Give the position of every Plasmodium parasite visible.
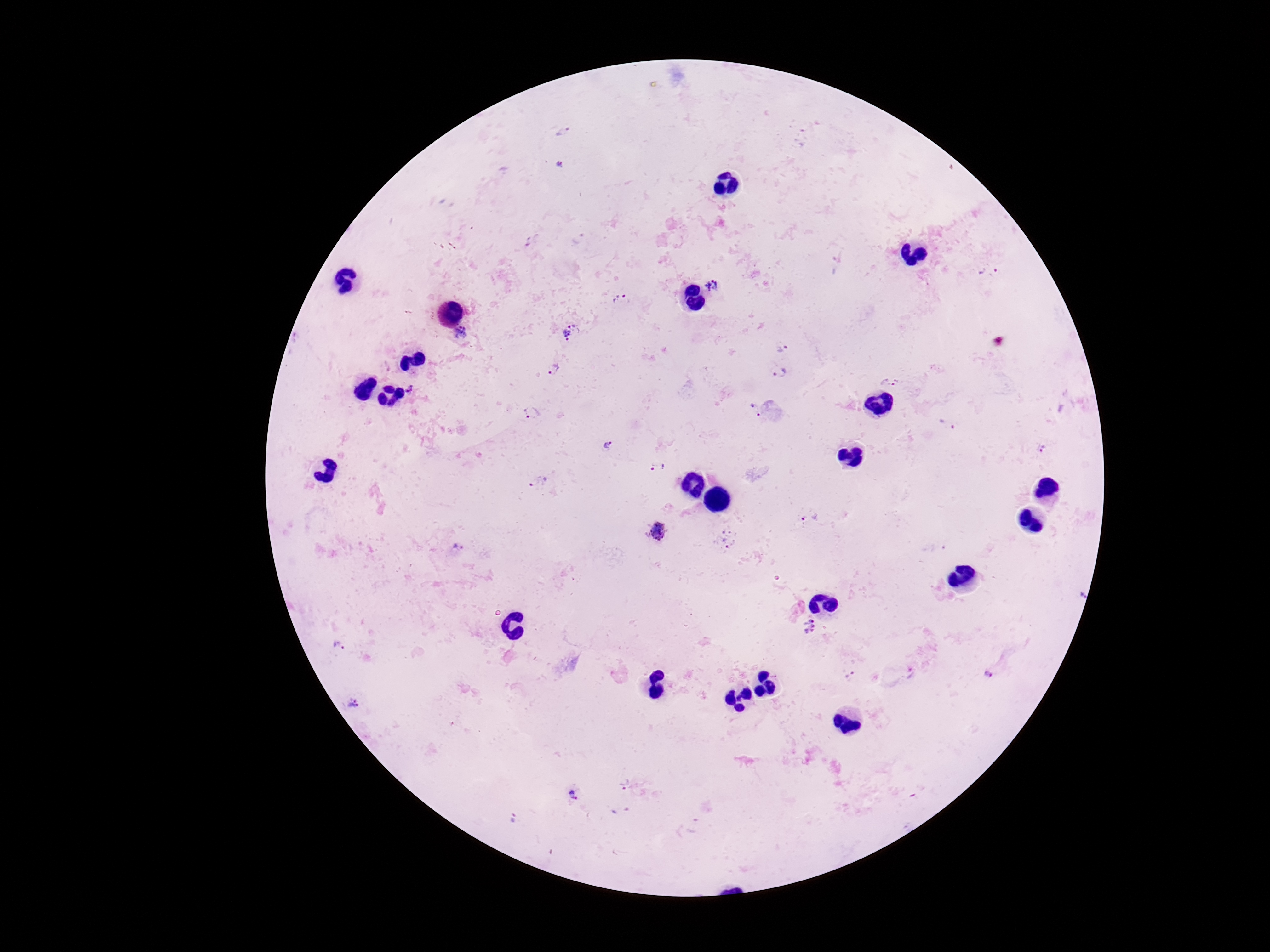

Approximate centers as [x, y] in pixels.
Plasmodium parasites: [562, 133], [559, 166], [532, 240], [987, 271], [712, 285], [621, 300], [461, 332], [571, 333], [782, 348], [553, 370], [779, 373], [890, 381], [411, 389], [755, 410], [533, 413], [947, 424], [608, 445], [1042, 449], [657, 466], [539, 483], [809, 518], [658, 532], [729, 540], [457, 551], [1080, 594], [810, 626], [339, 646], [987, 675], [850, 676], [353, 702], [625, 785], [573, 797], [513, 819].

100x magnification. Giemsa-stained preparation. Image is 1270×952 pixels. Photographed through the microscope eyepiece with a smartphone camera. Thick blood film. Patient malaria status: positive. One field from this slide.